Assess this cell for malaria.
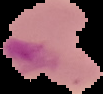

It is parasitized.

Summary:
  - Preparation: thin blood smear
  - Image size: 103×94 pixels
  - Image type: segmented cell region with the area outside set to black